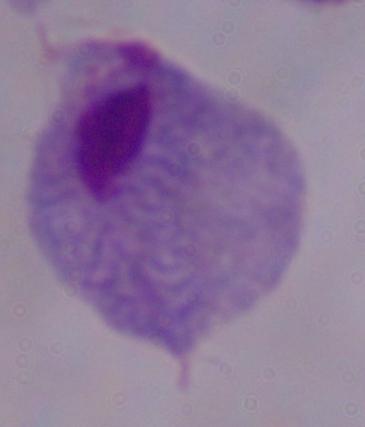
Captured at 1000x magnification. A trichomonad is shown. Photomicrograph.